Classify this cell by malaria status.
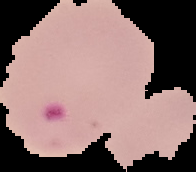
It is parasitized.

image size = 196×172 pixels
image type = segmented cell region on a black background
preparation = thin blood film